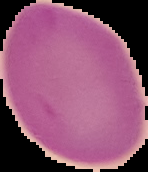
Image is 148×172 pixels. From a thin blood film. Segmented cell region on a black background. Malaria status: uninfected.